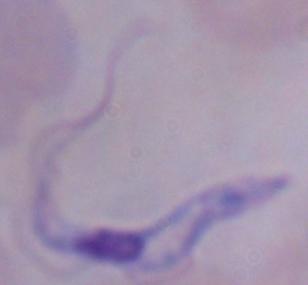

Captured at 1000x magnification. Photomicrograph. A trypanosome is shown.